Name the parasite shown.
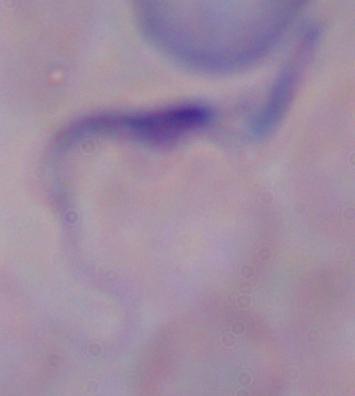

A trypanosome.

Summary:
  - Modality: micrograph
  - Magnification: 1000x